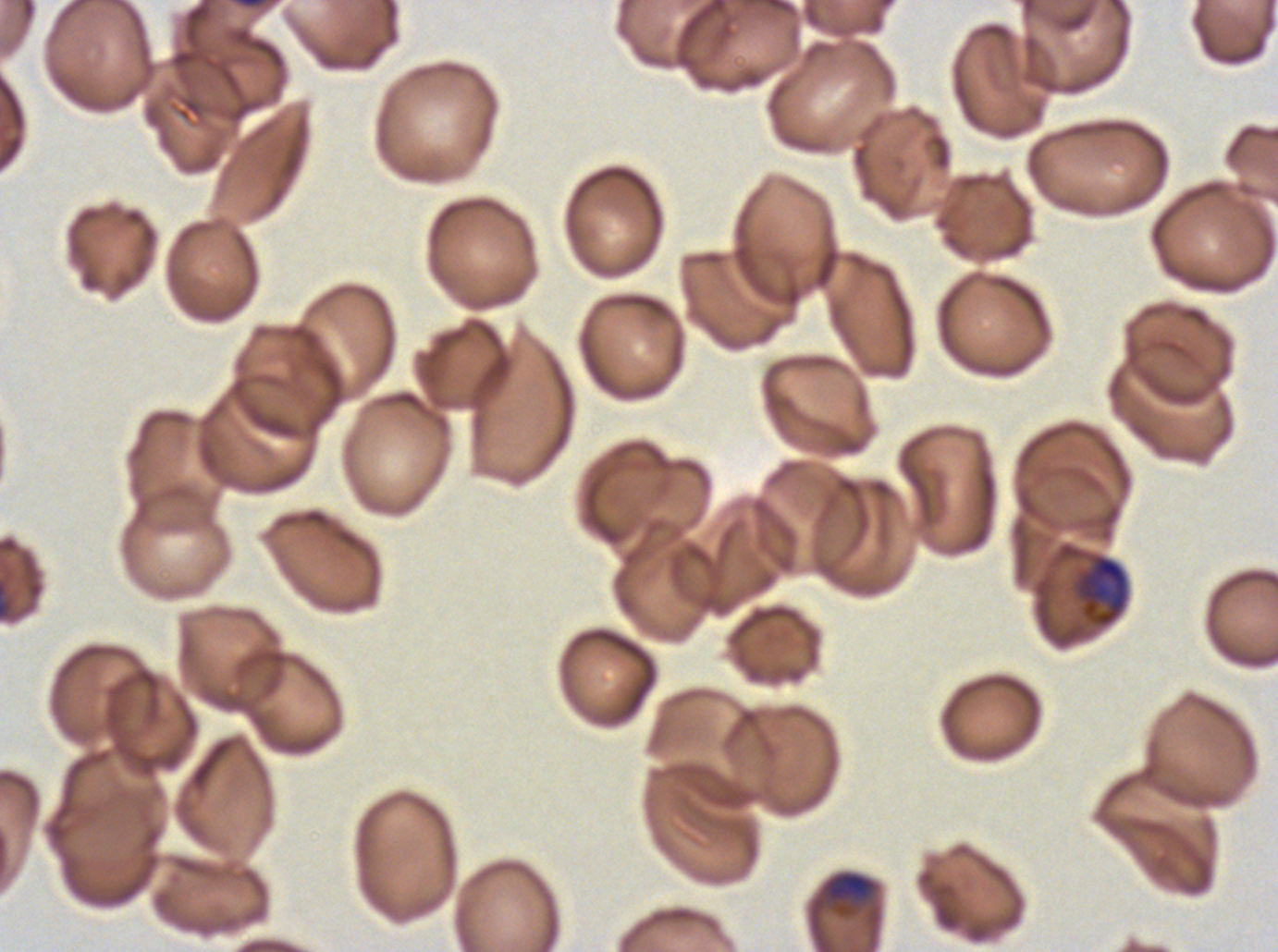 Approximate bounding boxes as {x1, y1, x2, y2} in pixels. Late trophozoite locations: {1055, 542, 1130, 629}, {821, 871, 878, 917}. Thin blood smear. Plasmodium falciparum cultured ex vivo for 24 to 48 hours, from a patient in The Gambia. One sub-image of a larger composite. Image is 1278×952 pixels. Giemsa stain.